Outline each blood parasite and name the species.
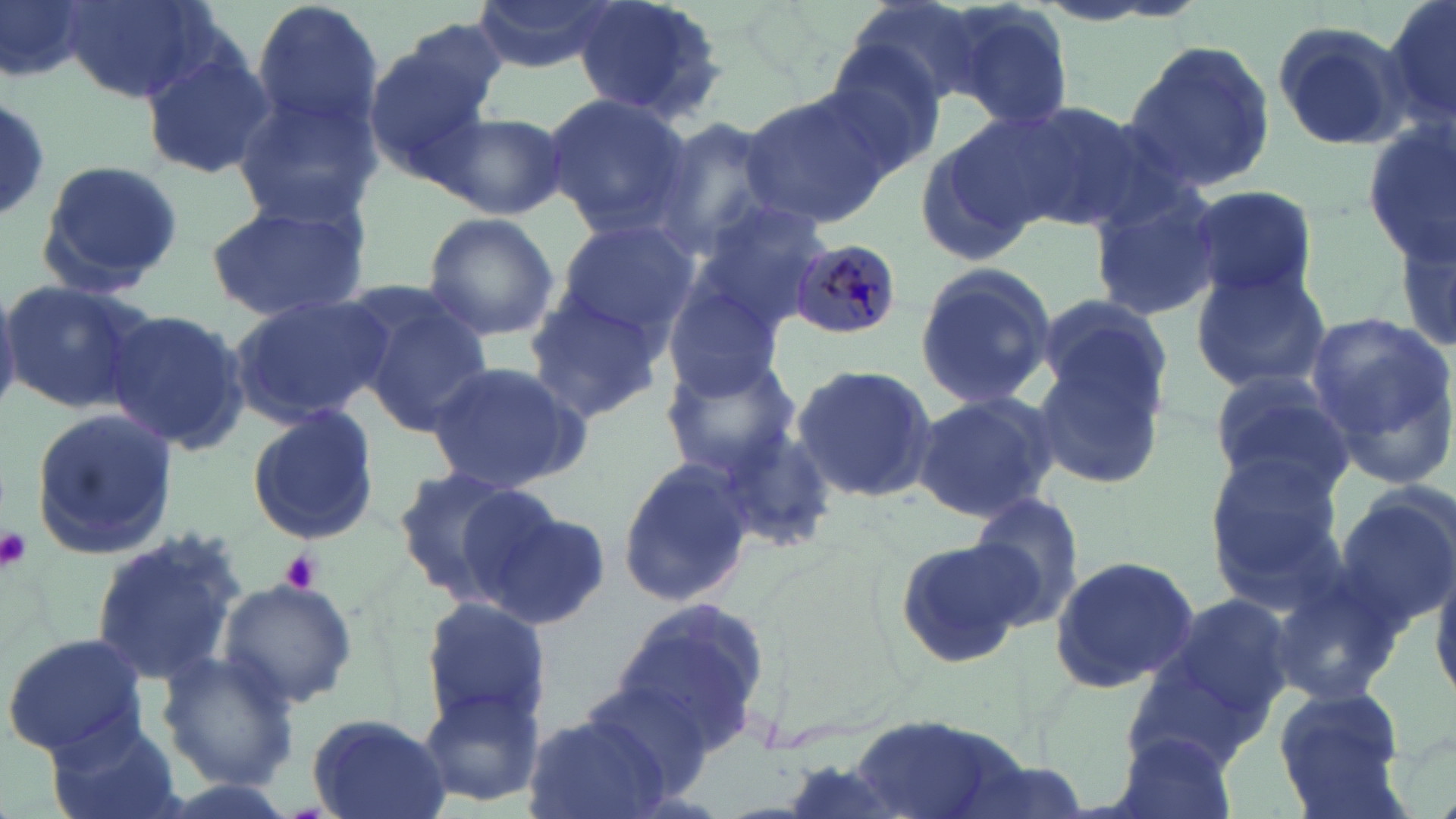
Approximate bounding boxes as (x1,y1)-(x2,y2) corner pairs in pixels.
Plasmodium malariae-infected red blood cells: (794,240)-(896,335).
No Plasmodium falciparum, Plasmodium ovale, Plasmodium vivax, Babesia divergens, or Trypanosoma brucei observed.

Platelet locations: (0,524)-(31,574), (279,549)-(324,594). Uninfected red blood cell locations: (1,0)-(92,86), (61,0)-(212,104), (251,0)-(384,137), (474,0)-(617,74), (572,0)-(727,124), (1384,0)-(1455,139), (937,2)-(1077,128), (1268,20)-(1410,151), (1123,36)-(1280,195), (819,41)-(947,171), (362,43)-(494,173), (138,44)-(274,180), (736,88)-(895,230), (232,91)-(382,225), (544,93)-(693,237), (0,99)-(53,222), (1002,101)-(1155,232), (435,111)-(565,219), (646,118)-(788,260), (1361,121)-(1456,265), (913,122)-(1051,265), (33,157)-(184,296), (1085,179)-(1226,321), (1185,184)-(1318,303), (202,197)-(370,322), (682,197)-(830,331), (420,211)-(559,342), (1392,211)-(1454,366), (551,218)-(699,344), (913,261)-(1060,412), (1189,265)-(1332,393), (3,279)-(150,413), (663,286)-(786,402), (227,293)-(390,427), (1031,293)-(1171,418), (521,295)-(667,421), (364,303)-(495,437), (103,308)-(249,454), (1305,310)-(1456,485), (1030,343)-(1170,487), (659,353)-(802,479), (422,360)-(591,497), (789,365)-(938,505), (1208,370)-(1354,498), (912,391)-(1059,523), (245,406)-(381,545), (27,407)-(179,560), (714,427)-(837,554), (616,454)-(755,606), (1204,460)-(1350,607), (389,466)-(538,604), (1333,483)-(1455,636), (965,491)-(1088,627), (467,498)-(609,628), (87,526)-(246,687), (893,532)-(1036,671), (1049,555)-(1198,691), (1431,567)-(1456,703), (1266,570)-(1408,706), (216,578)-(358,709), (1143,589)-(1296,729), (419,597)-(551,728), (612,597)-(771,748), (2,632)-(150,758), (1118,637)-(1281,773), (153,651)-(301,790), (580,678)-(720,793), (414,684)-(547,811), (1270,687)-(1410,816), (521,712)-(677,819), (305,713)-(451,819), (846,715)-(1029,819), (44,716)-(187,819), (1109,731)-(1239,819), (773,757)-(918,819). Slide-level diagnosis: Plasmodium malariae. May-Grünwald-Giemsa-stained preparation. Captured at 1000x magnification. Single field of view. Light microscopy. Image is 1456×819 pixels. Thin blood smear.